Identify the parasite.
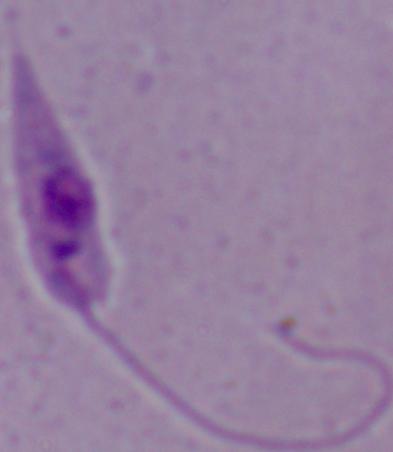
This is Leishmania.

Captured at 1000x magnification. Micrograph.